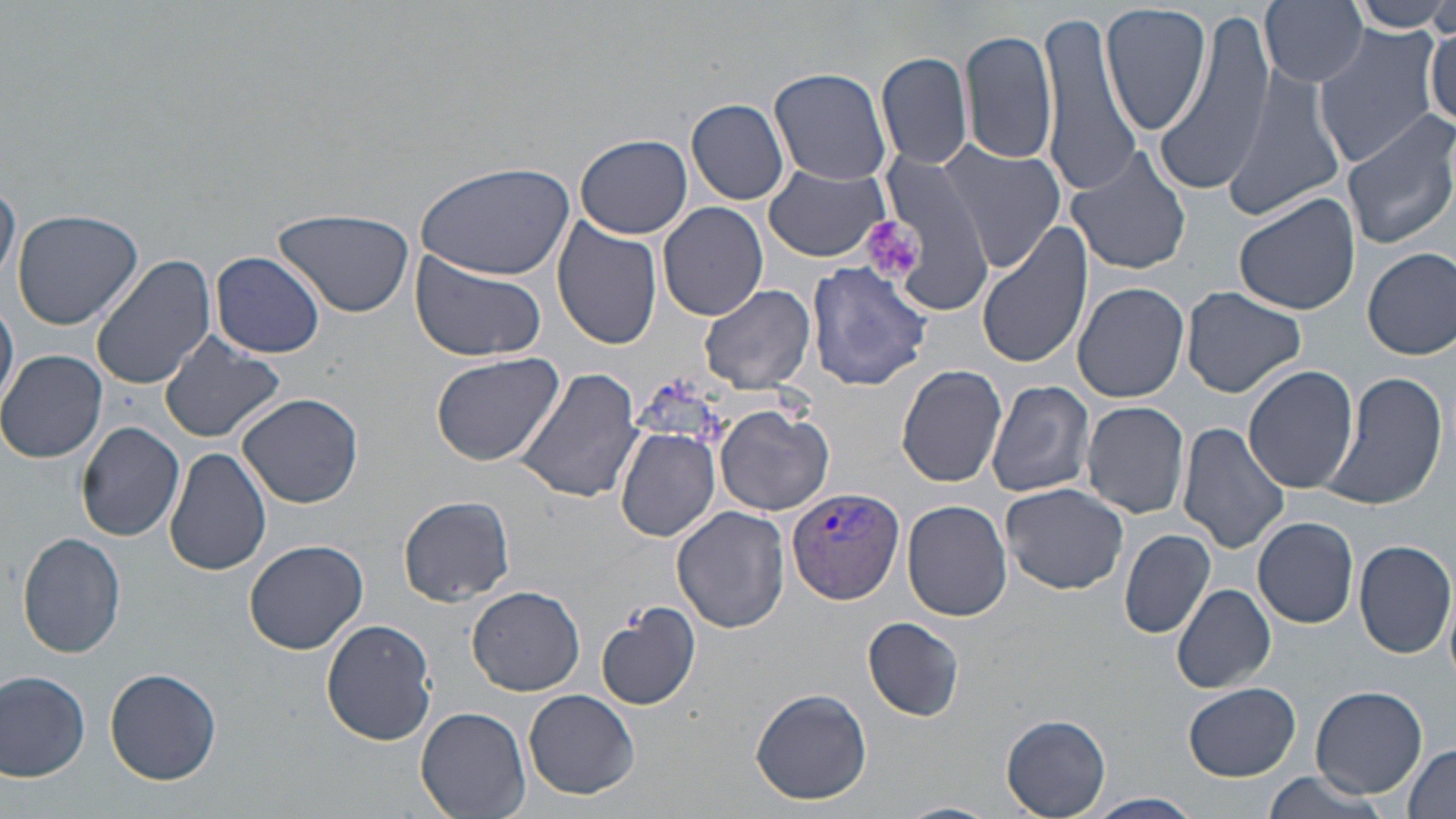

Summary:
  - Coordinate format: approximate bounding boxes as [x1, y1, x2, y2] in pixels
  - Plasmodium vivax-infected red blood cell locations: [784, 486, 905, 603]
  - Platelet locations: [863, 215, 925, 282]
  - Uninfected red blood cell locations: [1261, 0, 1369, 88], [1349, 0, 1456, 32], [1100, 3, 1211, 135], [1036, 11, 1141, 196], [1151, 12, 1275, 198], [961, 22, 1056, 171], [1426, 24, 1455, 130], [1312, 25, 1440, 169], [877, 52, 972, 169], [1220, 65, 1345, 222], [769, 68, 893, 186], [687, 97, 790, 205], [1340, 112, 1456, 249], [574, 133, 692, 239], [937, 142, 1065, 269], [1064, 143, 1195, 277], [877, 155, 994, 310], [411, 161, 574, 279], [764, 164, 894, 263], [0, 178, 19, 291], [1233, 190, 1360, 316], [659, 201, 769, 321], [11, 208, 144, 329], [275, 209, 415, 318], [551, 221, 664, 352], [975, 224, 1094, 370], [1363, 246, 1456, 361], [410, 249, 548, 362], [210, 252, 325, 358], [92, 255, 215, 394], [806, 260, 932, 390], [1073, 280, 1190, 403], [698, 283, 815, 394], [1180, 289, 1308, 398], [0, 300, 20, 410], [157, 333, 285, 444], [0, 349, 108, 463], [430, 352, 565, 465], [896, 363, 1009, 487], [513, 365, 643, 504], [1243, 367, 1358, 497], [1319, 371, 1448, 514], [986, 379, 1096, 498], [237, 393, 365, 508], [1080, 400, 1192, 518], [716, 404, 835, 514], [77, 422, 184, 540], [1177, 422, 1290, 556], [616, 428, 721, 542], [164, 446, 272, 576], [1000, 483, 1132, 597], [399, 496, 515, 605], [902, 500, 1012, 621], [672, 505, 792, 634], [1253, 516, 1358, 628], [1119, 528, 1215, 639], [17, 531, 127, 659], [243, 539, 369, 654], [1355, 540, 1455, 659], [1172, 582, 1276, 694], [467, 587, 585, 695], [596, 603, 701, 712], [863, 616, 965, 722], [320, 619, 437, 746], [105, 667, 222, 785], [0, 668, 92, 781], [1184, 682, 1301, 781], [1311, 685, 1428, 798], [522, 688, 640, 800], [750, 689, 872, 805], [417, 706, 530, 819], [1002, 714, 1111, 817], [1400, 744, 1455, 819], [1261, 770, 1393, 819], [1085, 792, 1203, 819]
  - Slide-level diagnosis: Plasmodium vivax
  - Field of view: single
  - Image size: 1456×819 pixels
  - Preparation: thin blood film
  - Stain: May-Grünwald-Giemsa
  - Magnification: 1000x
  - Modality: optical microscopy